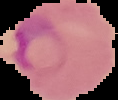
malaria status = parasitized
image size = 118×100 pixels
image type = cell region segmented out of the field of view; surrounding area masked to black
preparation = thin blood film